Assess this cell for malaria.
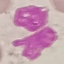
Uninfected.

Photographed with a smartphone camera at the microscope eyepiece. Cell patch, automatically extracted from a larger field of view and resized to 64 × 64 pixels. Giemsa stain. Thin smear of blood.